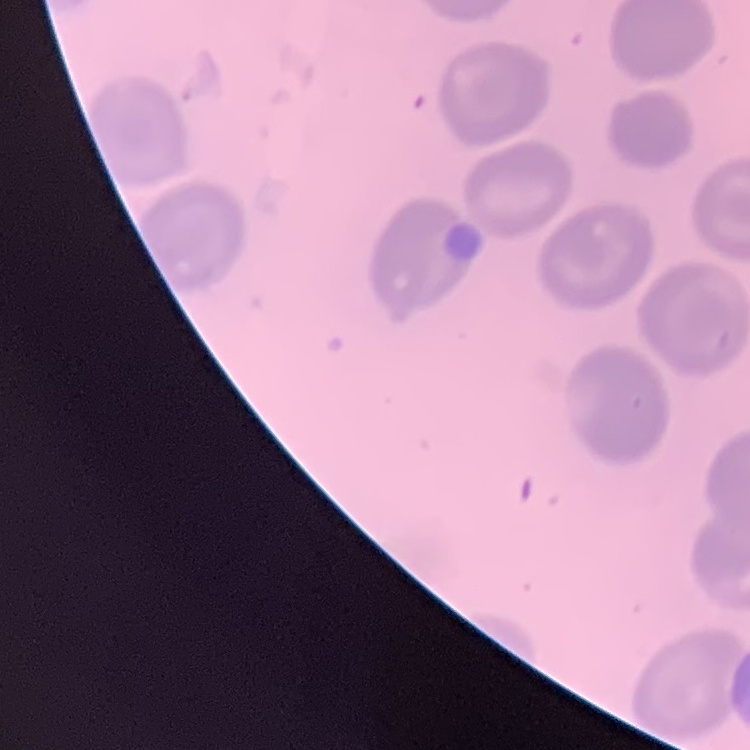
erythrocyte morphology = no rouleaux formation
stain = Field's or Giemsa
image type = square crop of a larger photomicrograph
preparation = thin peripheral smear